Assess the morphology of the erythrocytes.
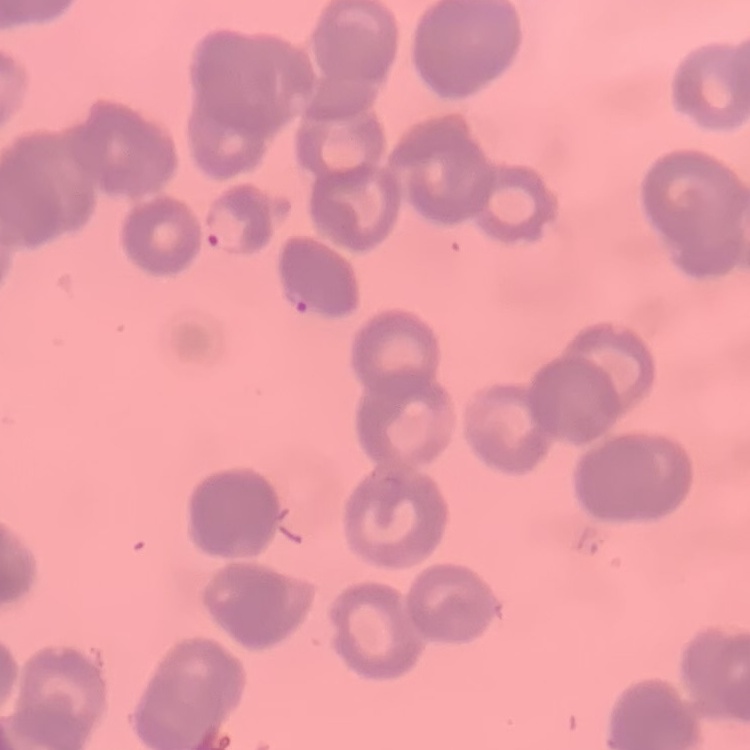

Rouleaux formation.

Square crop of a larger photomicrograph. Thin blood smear. Field's or Giemsa stain.